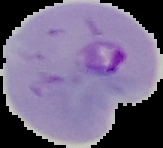

Summary:
  - Image type: segmented cell region with the area outside set to black
  - Preparation: thin blood film
  - Result: Plasmodium parasites identified
  - Image size: 163×148 pixels